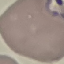

Result: malaria parasites detected. Giemsa-stained preparation. Photographed with a smartphone camera at the microscope eyepiece. Cell patch, automatically extracted from a larger field of view and resized to 64 × 64 pixels. Thin blood smear.